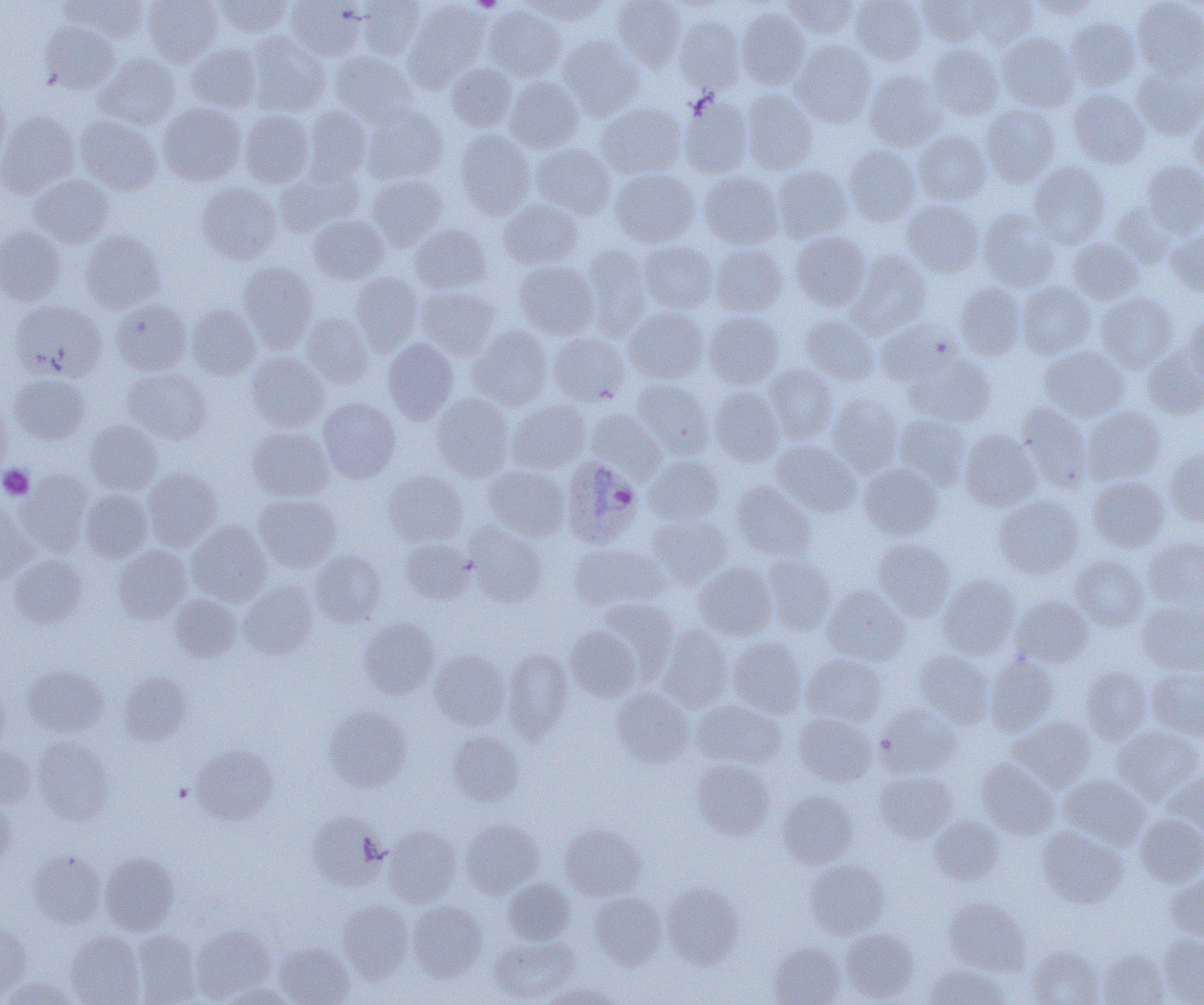
{
  "slide_level_diagnosis": "Plasmodium ovale",
  "preparation": "thin blood smear",
  "plasmodium_ovale_infected_red_blood_cell_locations": "approximate bounding boxes as named x1/y1/x2/y2 corners in pixels: (x1=560, y1=456, x2=643, y2=548)",
  "magnification": "1000x",
  "uninfected_red_blood_cell_locations": "approximate bounding boxes as named x1/y1/x2/y2 corners in pixels: (x1=62, y1=0, x2=150, y2=42), (x1=143, y1=0, x2=222, y2=66), (x1=213, y1=0, x2=294, y2=38), (x1=285, y1=0, x2=366, y2=61), (x1=358, y1=0, x2=426, y2=60), (x1=405, y1=0, x2=490, y2=86), (x1=524, y1=0, x2=607, y2=25), (x1=612, y1=0, x2=687, y2=70), (x1=782, y1=0, x2=860, y2=38), (x1=850, y1=0, x2=926, y2=65), (x1=917, y1=0, x2=989, y2=46), (x1=968, y1=0, x2=1038, y2=48), (x1=1030, y1=0, x2=1100, y2=19), (x1=1132, y1=0, x2=1204, y2=77), (x1=484, y1=4, x2=566, y2=81), (x1=736, y1=8, x2=810, y2=89), (x1=675, y1=15, x2=745, y2=92), (x1=1066, y1=16, x2=1140, y2=90), (x1=41, y1=23, x2=120, y2=93), (x1=247, y1=32, x2=330, y2=115), (x1=997, y1=32, x2=1078, y2=111), (x1=558, y1=35, x2=644, y2=118), (x1=790, y1=40, x2=876, y2=127), (x1=186, y1=43, x2=261, y2=112), (x1=926, y1=44, x2=1004, y2=119), (x1=331, y1=52, x2=417, y2=126), (x1=96, y1=53, x2=180, y2=129), (x1=446, y1=62, x2=517, y2=131), (x1=1131, y1=64, x2=1204, y2=138), (x1=864, y1=71, x2=947, y2=151), (x1=504, y1=76, x2=584, y2=152), (x1=741, y1=88, x2=818, y2=175), (x1=1068, y1=89, x2=1150, y2=168), (x1=0, y1=91, x2=10, y2=171), (x1=680, y1=95, x2=754, y2=178), (x1=158, y1=102, x2=245, y2=185), (x1=597, y1=103, x2=686, y2=179), (x1=981, y1=104, x2=1060, y2=187), (x1=303, y1=106, x2=372, y2=183), (x1=362, y1=106, x2=449, y2=184), (x1=239, y1=109, x2=314, y2=187), (x1=1188, y1=109, x2=1204, y2=177), (x1=0, y1=110, x2=79, y2=197), (x1=75, y1=115, x2=162, y2=195), (x1=912, y1=129, x2=992, y2=206), (x1=454, y1=130, x2=535, y2=218), (x1=530, y1=143, x2=615, y2=217), (x1=843, y1=145, x2=921, y2=225), (x1=1140, y1=160, x2=1204, y2=237), (x1=1029, y1=163, x2=1109, y2=248), (x1=772, y1=165, x2=852, y2=243), (x1=276, y1=166, x2=362, y2=235), (x1=610, y1=168, x2=699, y2=247), (x1=699, y1=171, x2=783, y2=249), (x1=29, y1=174, x2=113, y2=247), (x1=367, y1=174, x2=448, y2=249), (x1=196, y1=182, x2=282, y2=264), (x1=498, y1=199, x2=582, y2=268), (x1=903, y1=199, x2=984, y2=277), (x1=1110, y1=202, x2=1178, y2=268), (x1=979, y1=208, x2=1059, y2=291), (x1=308, y1=215, x2=388, y2=283), (x1=410, y1=224, x2=491, y2=294), (x1=0, y1=228, x2=65, y2=304), (x1=80, y1=230, x2=164, y2=311), (x1=1167, y1=230, x2=1204, y2=295), (x1=790, y1=232, x2=871, y2=310), (x1=1068, y1=238, x2=1143, y2=304), (x1=640, y1=240, x2=717, y2=312), (x1=710, y1=244, x2=787, y2=316), (x1=583, y1=245, x2=651, y2=339), (x1=847, y1=250, x2=931, y2=337), (x1=238, y1=261, x2=318, y2=351), (x1=514, y1=261, x2=600, y2=338), (x1=351, y1=272, x2=423, y2=355), (x1=1017, y1=281, x2=1096, y2=358), (x1=955, y1=282, x2=1027, y2=360), (x1=416, y1=286, x2=498, y2=359), (x1=1096, y1=292, x2=1178, y2=372), (x1=112, y1=299, x2=191, y2=375), (x1=10, y1=300, x2=107, y2=380), (x1=187, y1=304, x2=260, y2=380), (x1=625, y1=307, x2=709, y2=383), (x1=704, y1=311, x2=785, y2=388), (x1=301, y1=312, x2=373, y2=388), (x1=799, y1=314, x2=879, y2=385), (x1=1182, y1=314, x2=1204, y2=383), (x1=876, y1=318, x2=961, y2=387), (x1=467, y1=325, x2=553, y2=410), (x1=548, y1=332, x2=631, y2=406), (x1=382, y1=338, x2=458, y2=424), (x1=1040, y1=346, x2=1129, y2=421), (x1=1142, y1=346, x2=1204, y2=419), (x1=246, y1=351, x2=329, y2=431), (x1=905, y1=352, x2=995, y2=427), (x1=765, y1=364, x2=838, y2=443), (x1=123, y1=368, x2=212, y2=443), (x1=9, y1=373, x2=90, y2=443), (x1=632, y1=377, x2=714, y2=458), (x1=709, y1=386, x2=785, y2=465), (x1=827, y1=392, x2=903, y2=475), (x1=432, y1=393, x2=514, y2=481), (x1=0, y1=397, x2=10, y2=479), (x1=318, y1=397, x2=401, y2=482), (x1=507, y1=399, x2=591, y2=474), (x1=1017, y1=403, x2=1092, y2=491), (x1=1082, y1=406, x2=1165, y2=484), (x1=586, y1=409, x2=664, y2=480), (x1=895, y1=413, x2=971, y2=488), (x1=85, y1=420, x2=163, y2=494), (x1=247, y1=425, x2=334, y2=501), (x1=959, y1=430, x2=1041, y2=511), (x1=771, y1=441, x2=861, y2=516), (x1=1164, y1=448, x2=1204, y2=526), (x1=644, y1=455, x2=725, y2=525), (x1=859, y1=464, x2=943, y2=540), (x1=485, y1=465, x2=570, y2=540), (x1=143, y1=467, x2=222, y2=550), (x1=17, y1=470, x2=94, y2=556), (x1=383, y1=470, x2=468, y2=546), (x1=1087, y1=476, x2=1169, y2=551), (x1=731, y1=481, x2=815, y2=561), (x1=80, y1=489, x2=152, y2=562), (x1=253, y1=494, x2=341, y2=571), (x1=994, y1=495, x2=1084, y2=577), (x1=0, y1=503, x2=37, y2=584), (x1=646, y1=513, x2=731, y2=588), (x1=187, y1=520, x2=272, y2=606), (x1=465, y1=523, x2=547, y2=607), (x1=1143, y1=537, x2=1204, y2=608), (x1=873, y1=538, x2=955, y2=620), (x1=400, y1=539, x2=475, y2=604), (x1=570, y1=542, x2=669, y2=612), (x1=113, y1=545, x2=192, y2=623), (x1=310, y1=550, x2=385, y2=627), (x1=8, y1=554, x2=86, y2=627), (x1=761, y1=554, x2=836, y2=635), (x1=1071, y1=555, x2=1148, y2=630), (x1=694, y1=563, x2=777, y2=639), (x1=937, y1=575, x2=1020, y2=658), (x1=239, y1=581, x2=318, y2=658), (x1=822, y1=585, x2=910, y2=665), (x1=170, y1=594, x2=242, y2=662), (x1=1012, y1=595, x2=1093, y2=666), (x1=597, y1=598, x2=678, y2=679), (x1=1138, y1=601, x2=1204, y2=675), (x1=359, y1=616, x2=440, y2=699), (x1=657, y1=624, x2=733, y2=711), (x1=566, y1=626, x2=643, y2=701), (x1=728, y1=636, x2=806, y2=717), (x1=429, y1=649, x2=510, y2=729), (x1=502, y1=649, x2=573, y2=743), (x1=914, y1=649, x2=994, y2=727), (x1=801, y1=653, x2=887, y2=726), (x1=985, y1=654, x2=1058, y2=736), (x1=23, y1=664, x2=108, y2=736), (x1=1081, y1=667, x2=1151, y2=744), (x1=1147, y1=667, x2=1204, y2=740), (x1=119, y1=671, x2=191, y2=745), (x1=0, y1=686, x2=9, y2=755), (x1=611, y1=688, x2=694, y2=767), (x1=692, y1=700, x2=787, y2=768), (x1=876, y1=703, x2=960, y2=778), (x1=325, y1=706, x2=412, y2=791), (x1=793, y1=713, x2=876, y2=786), (x1=1010, y1=716, x2=1096, y2=790), (x1=1111, y1=726, x2=1203, y2=804), (x1=447, y1=730, x2=524, y2=806), (x1=33, y1=736, x2=114, y2=823), (x1=192, y1=744, x2=277, y2=824), (x1=0, y1=747, x2=36, y2=807), (x1=977, y1=759, x2=1059, y2=838), (x1=691, y1=760, x2=775, y2=839), (x1=1163, y1=769, x2=1204, y2=838), (x1=876, y1=771, x2=956, y2=843), (x1=1058, y1=774, x2=1150, y2=849), (x1=777, y1=789, x2=859, y2=868), (x1=0, y1=796, x2=15, y2=870), (x1=308, y1=812, x2=385, y2=888), (x1=1135, y1=813, x2=1204, y2=887), (x1=929, y1=815, x2=1003, y2=884), (x1=460, y1=818, x2=543, y2=897), (x1=559, y1=823, x2=647, y2=901), (x1=384, y1=825, x2=461, y2=906), (x1=1037, y1=826, x2=1127, y2=907), (x1=28, y1=849, x2=106, y2=928), (x1=100, y1=852, x2=179, y2=934), (x1=805, y1=859, x2=889, y2=938), (x1=1167, y1=870, x2=1204, y2=941), (x1=503, y1=878, x2=575, y2=944), (x1=663, y1=882, x2=745, y2=968), (x1=590, y1=892, x2=666, y2=969), (x1=944, y1=897, x2=1031, y2=975), (x1=337, y1=900, x2=413, y2=981), (x1=408, y1=901, x2=488, y2=981), (x1=0, y1=921, x2=32, y2=997), (x1=191, y1=923, x2=275, y2=1001), (x1=841, y1=927, x2=919, y2=1002), (x1=66, y1=930, x2=145, y2=1005), (x1=130, y1=931, x2=202, y2=1004), (x1=1157, y1=933, x2=1204, y2=1004), (x1=490, y1=935, x2=579, y2=1003), (x1=768, y1=941, x2=845, y2=1005), (x1=272, y1=942, x2=355, y2=1005), (x1=1028, y1=945, x2=1105, y2=1005), (x1=1099, y1=949, x2=1170, y2=1005), (x1=923, y1=963, x2=1010, y2=1005), (x1=2, y1=977, x2=79, y2=1005), (x1=218, y1=982, x2=298, y2=1005), (x1=543, y1=983, x2=622, y2=1005)",
  "modality": "light microscopy",
  "field_of_view": "single",
  "platelet_locations": "approximate bounding boxes as named x1/y1/x2/y2 corners in pixels: (x1=470, y1=0, x2=503, y2=12), (x1=0, y1=464, x2=34, y2=500), (x1=175, y1=783, x2=192, y2=801)",
  "image_size": "1204×1005 pixels"
}